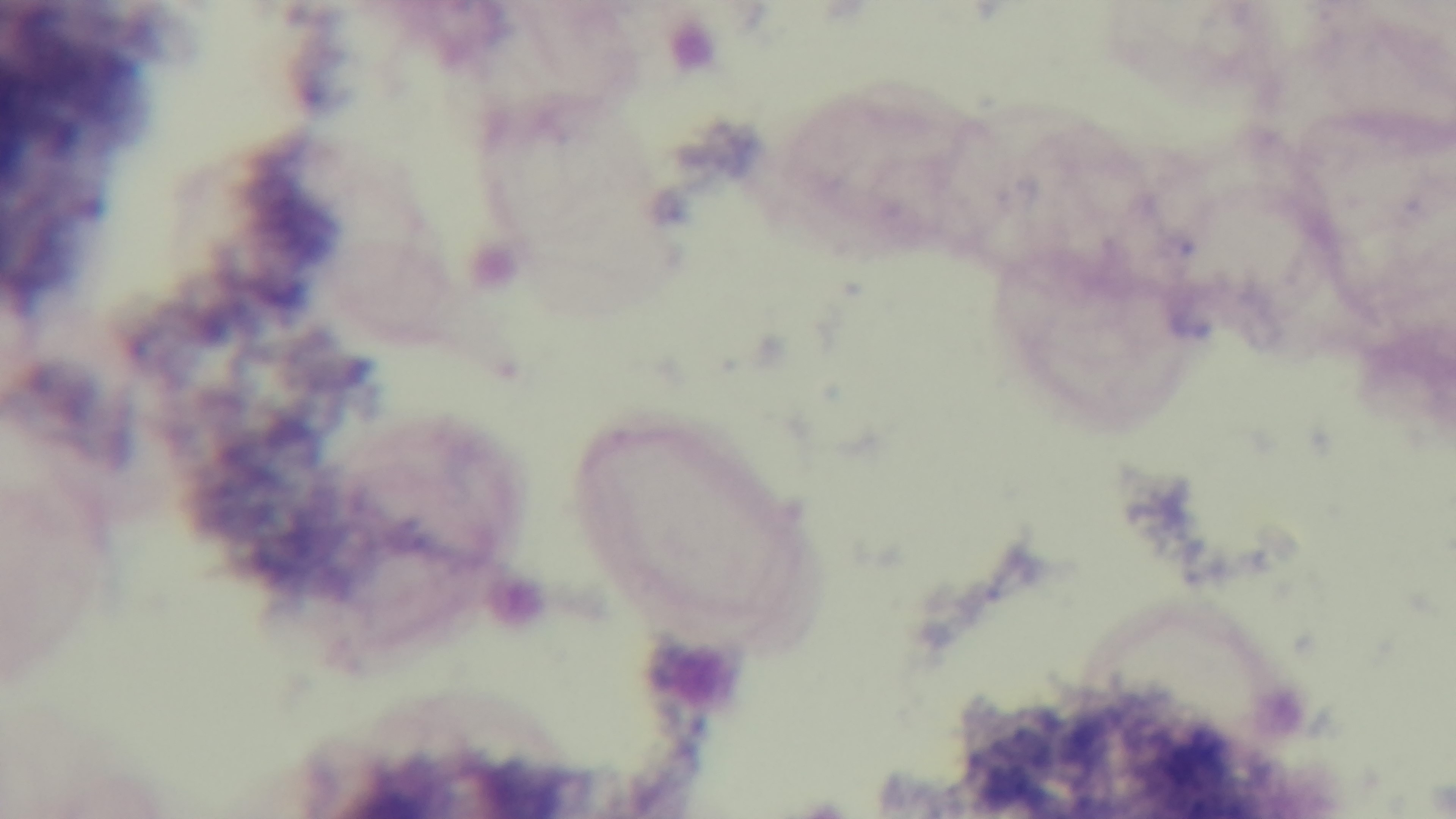

Summary:
  - Capture: mounted 4K digital camera
  - Preparation: thick
  - Malaria status: uninfected
  - Field of view: single
  - Stain: Giemsa
  - Objective: 100x oil immersion
  - Modality: light microscopy